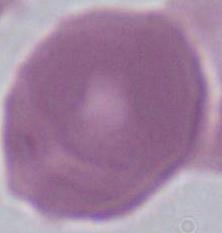

magnification = 1000x
modality = photomicrograph
identification = erythrocyte